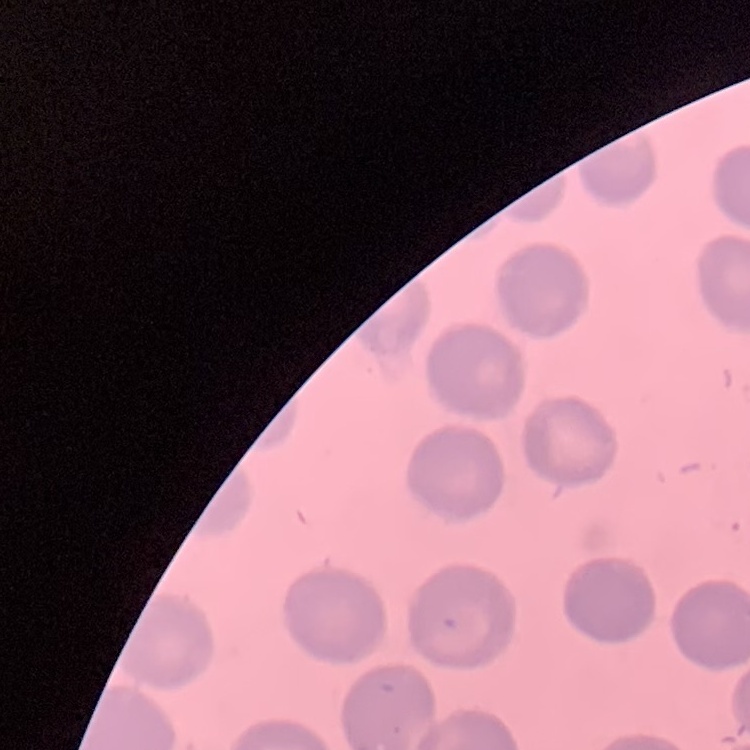
erythrocyte_morphology: no rouleaux formation
stain: Field's or Giemsa
image_type: one tile cut from a larger photomicrograph
preparation: thin peripheral smear